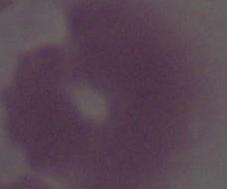
modality: photomicrograph
magnification: 1000x
identification: erythrocyte